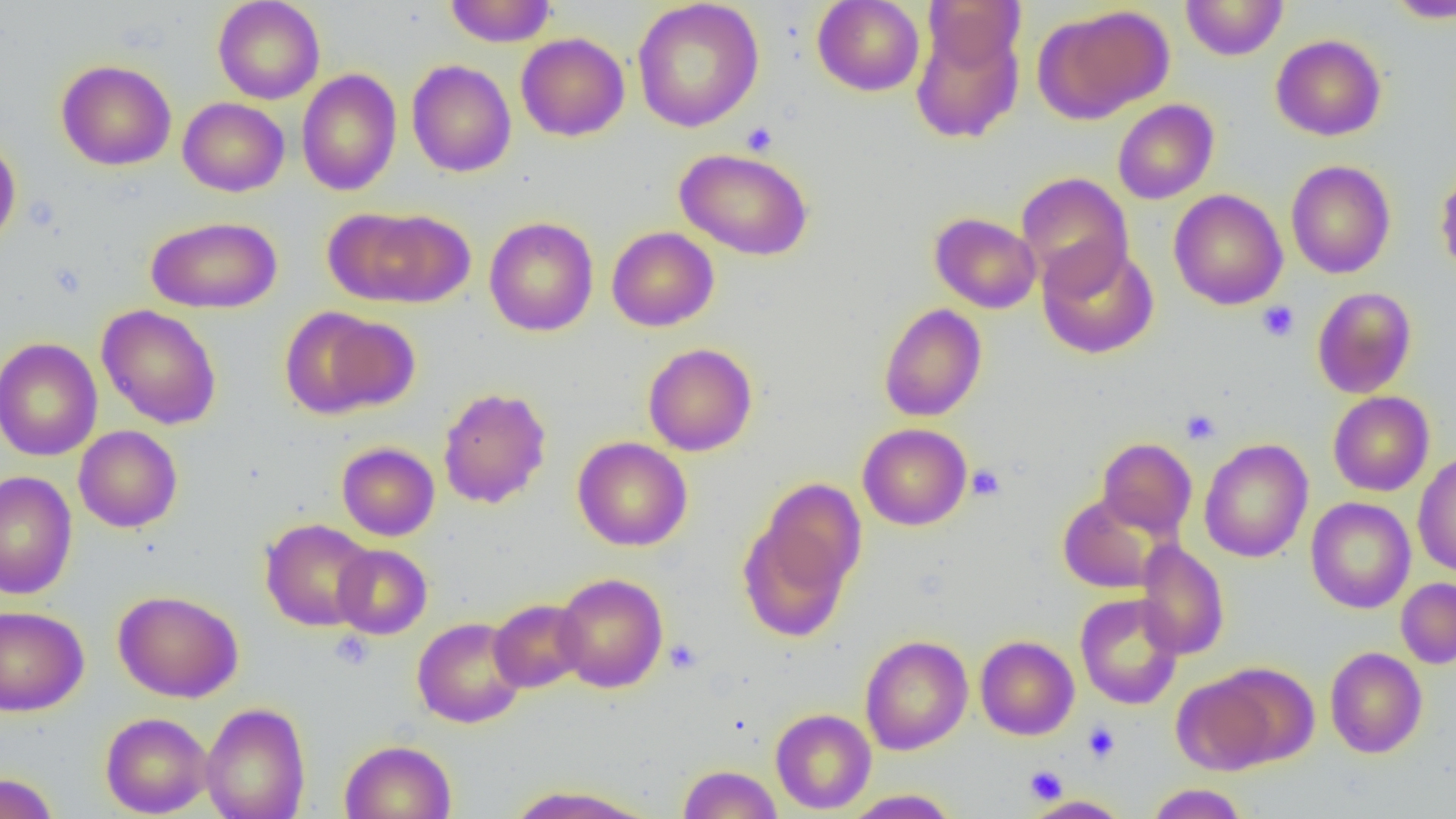

Summary:
  - Coordinate format: approximate bounding boxes as named x1/y1/x2/y2 corners in pixels
  - Platelet locations: (x1=740, y1=123, x2=778, y2=155), (x1=1257, y1=301, x2=1299, y2=341), (x1=1181, y1=409, x2=1221, y2=445), (x1=968, y1=464, x2=1005, y2=501), (x1=329, y1=630, x2=375, y2=670), (x1=664, y1=638, x2=702, y2=674), (x1=1082, y1=722, x2=1120, y2=763), (x1=1024, y1=765, x2=1068, y2=804)
  - Uninfected red blood cell locations: (x1=213, y1=0, x2=325, y2=104), (x1=444, y1=0, x2=556, y2=47), (x1=812, y1=0, x2=925, y2=96), (x1=924, y1=0, x2=1025, y2=72), (x1=1180, y1=0, x2=1289, y2=60), (x1=1384, y1=0, x2=1456, y2=23), (x1=632, y1=1, x2=764, y2=132), (x1=1035, y1=5, x2=1174, y2=124), (x1=910, y1=20, x2=1025, y2=143), (x1=516, y1=33, x2=629, y2=141), (x1=1271, y1=34, x2=1386, y2=141), (x1=56, y1=59, x2=177, y2=170), (x1=406, y1=59, x2=516, y2=177), (x1=296, y1=68, x2=402, y2=196), (x1=178, y1=97, x2=289, y2=197), (x1=1112, y1=99, x2=1219, y2=204), (x1=0, y1=136, x2=22, y2=251), (x1=674, y1=147, x2=814, y2=261), (x1=1285, y1=160, x2=1395, y2=279), (x1=1434, y1=165, x2=1456, y2=279), (x1=1016, y1=172, x2=1134, y2=292), (x1=1169, y1=189, x2=1288, y2=310), (x1=327, y1=206, x2=475, y2=308), (x1=930, y1=212, x2=1041, y2=313), (x1=145, y1=216, x2=283, y2=314), (x1=484, y1=216, x2=599, y2=336), (x1=607, y1=226, x2=719, y2=331), (x1=1037, y1=241, x2=1159, y2=359), (x1=1311, y1=286, x2=1417, y2=398), (x1=878, y1=303, x2=987, y2=422), (x1=96, y1=304, x2=222, y2=430), (x1=278, y1=306, x2=411, y2=419), (x1=0, y1=337, x2=102, y2=462), (x1=642, y1=342, x2=758, y2=456), (x1=438, y1=387, x2=552, y2=509), (x1=1328, y1=391, x2=1434, y2=496), (x1=858, y1=423, x2=972, y2=530), (x1=73, y1=425, x2=183, y2=533), (x1=572, y1=436, x2=693, y2=551), (x1=1097, y1=437, x2=1197, y2=538), (x1=1199, y1=438, x2=1313, y2=563), (x1=337, y1=442, x2=440, y2=541), (x1=1413, y1=452, x2=1456, y2=576), (x1=1, y1=470, x2=78, y2=599), (x1=1058, y1=492, x2=1168, y2=594), (x1=1305, y1=497, x2=1416, y2=613), (x1=737, y1=507, x2=856, y2=643), (x1=260, y1=518, x2=376, y2=631), (x1=1135, y1=539, x2=1230, y2=660), (x1=333, y1=544, x2=432, y2=639), (x1=553, y1=572, x2=668, y2=693), (x1=1396, y1=577, x2=1456, y2=668), (x1=113, y1=590, x2=243, y2=702), (x1=1075, y1=593, x2=1184, y2=710), (x1=489, y1=598, x2=589, y2=693), (x1=0, y1=605, x2=89, y2=717), (x1=412, y1=616, x2=527, y2=728), (x1=860, y1=635, x2=973, y2=755), (x1=975, y1=635, x2=1079, y2=740), (x1=1325, y1=646, x2=1428, y2=758), (x1=1213, y1=663, x2=1320, y2=766), (x1=1173, y1=674, x2=1280, y2=775), (x1=201, y1=702, x2=310, y2=819), (x1=770, y1=708, x2=876, y2=814), (x1=100, y1=711, x2=213, y2=818), (x1=339, y1=739, x2=456, y2=819), (x1=677, y1=764, x2=783, y2=819), (x1=0, y1=772, x2=60, y2=819), (x1=1146, y1=783, x2=1249, y2=819), (x1=504, y1=785, x2=656, y2=819), (x1=841, y1=789, x2=961, y2=818), (x1=1023, y1=795, x2=1132, y2=819)
  - Slide-level diagnosis: negative for blood parasites
  - Preparation: thin blood film
  - Image size: 1456×819 pixels
  - Field of view: one of a larger specimen
  - Magnification: 1000x
  - Modality: light microscopy